Give the position of every Plasmodium parasite.
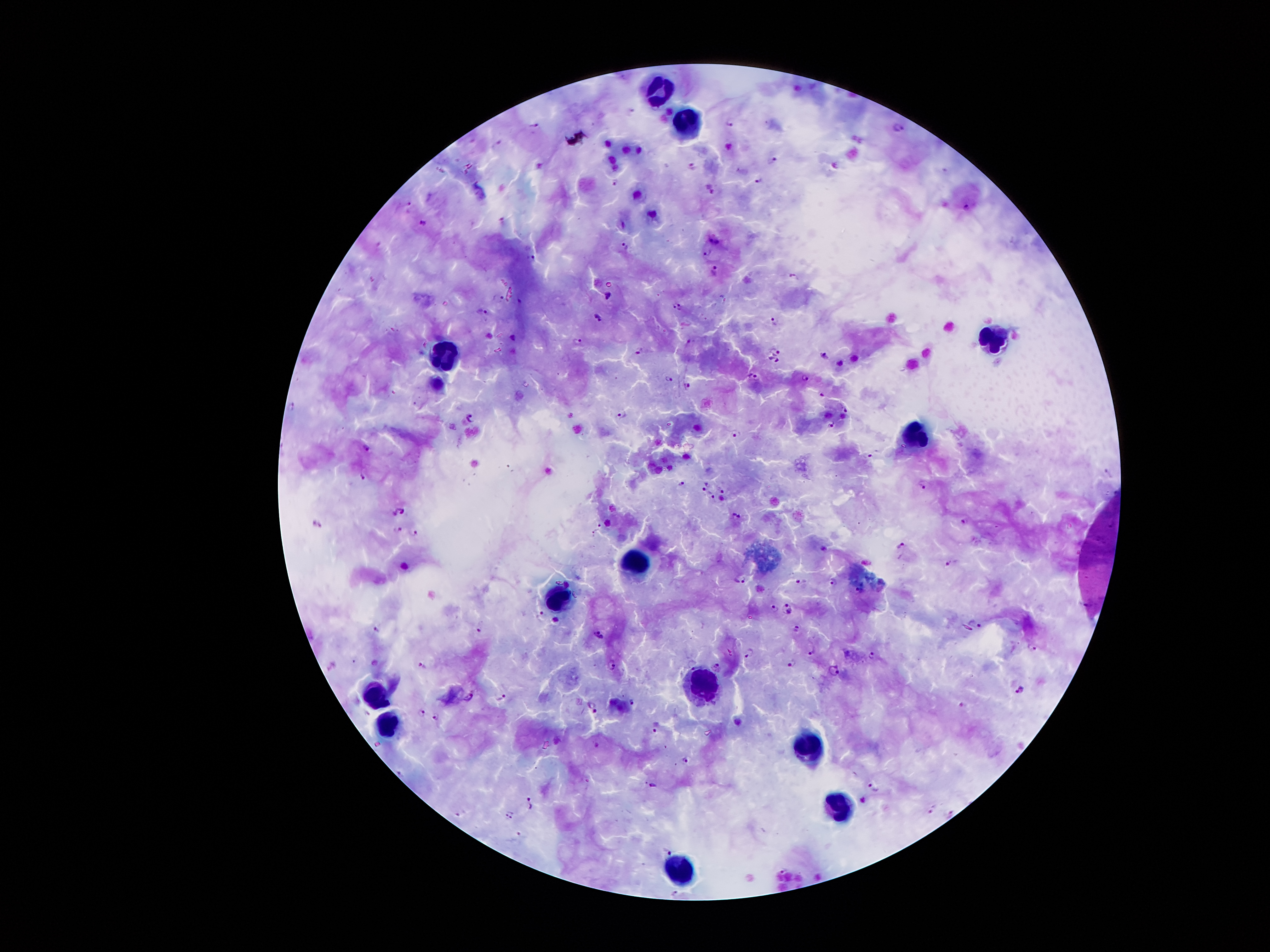
Approximate centers as (x, y) in pixels.
Plasmodium parasites: (630, 107), (730, 119), (536, 122), (899, 126), (498, 142), (773, 159), (693, 163), (758, 177), (615, 181), (710, 188), (968, 206), (503, 219), (422, 221), (714, 238), (625, 243), (707, 252), (533, 258), (714, 272), (794, 274), (608, 294), (500, 298), (518, 300), (677, 307), (482, 311), (597, 316), (773, 320), (513, 338), (579, 339), (689, 343), (775, 349), (638, 350), (825, 357), (774, 359), (754, 376), (669, 377), (805, 378), (687, 385), (822, 394), (292, 406), (845, 409), (622, 415), (470, 418), (832, 424), (734, 433), (366, 447), (869, 454), (363, 475), (683, 484), (921, 485), (704, 487), (721, 487), (714, 496), (404, 509), (395, 512), (739, 515), (965, 522), (317, 523), (600, 523), (399, 530), (414, 530), (596, 531), (900, 544), (949, 563), (742, 577), (802, 580), (832, 581), (857, 590), (786, 609), (774, 610), (541, 613), (555, 619), (976, 623), (480, 629), (795, 629), (378, 630), (599, 634), (1033, 647), (811, 650), (749, 653), (871, 656), (792, 663), (613, 664), (692, 664), (423, 665), (717, 667), (834, 670), (1018, 689), (503, 697), (632, 702), (592, 707), (421, 710), (436, 717), (656, 725), (686, 759), (650, 784), (875, 786), (531, 802), (931, 807), (510, 814), (948, 814), (667, 850).

{
  "magnification": "100x",
  "preparation": "thick blood film",
  "leukocyte_locations": "approximate centers as (x, y) in pixels: (659, 89), (685, 123), (992, 342), (442, 360), (910, 434), (634, 560), (561, 603), (703, 685), (374, 696), (389, 720), (807, 747), (841, 801), (682, 875)",
  "field_of_view": "one from this slide",
  "capture": "smartphone through the microscope eyepiece",
  "stain": "Giemsa",
  "patient_malaria_status": "infected with Plasmodium falciparum",
  "image_size": "1270×952 pixels"
}